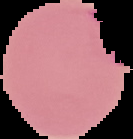
Summary:
  - Image type: cell region segmented out of the field of view; surrounding area masked to black
  - Preparation: thin blood smear
  - Result: Plasmodium parasites identified
  - Image size: 133×139 pixels